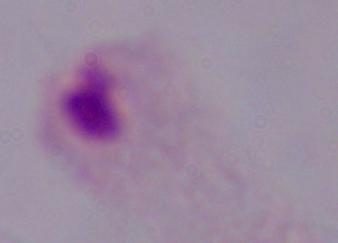

magnification = 1000x
identification = trichomonad
modality = micrograph